Give the position of every malaria parasite.
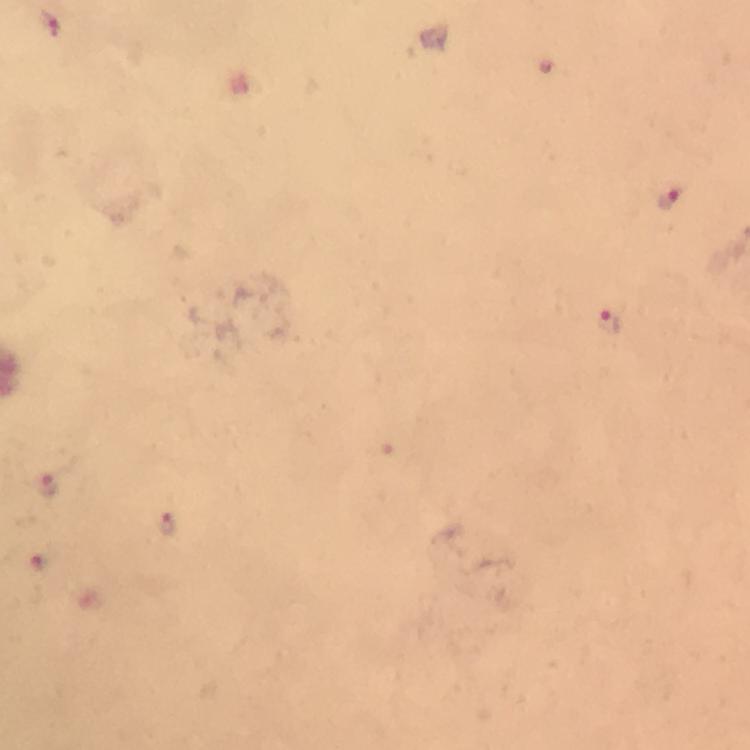

Approximate object centers, in pixels from the top-left corner.
Malaria parasites: (x=48, y=24), (x=670, y=197), (x=608, y=323), (x=49, y=489), (x=168, y=525), (x=41, y=560).

immersion oil = applied
image size = 750×750 pixels
magnification = 100x
cropped from = a single field of view
stain = Giemsa
context = from a diagnostic examination for malaria
preparation = thick smear
capture = smartphone camera through the microscope